Report the malaria status of this cell.
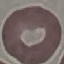

It is uninfected.

capture = smartphone through the microscope eyepiece
image type = automatically extracted cell patch, resized to 64 × 64 pixels
preparation = thin smear
stain = Giemsa